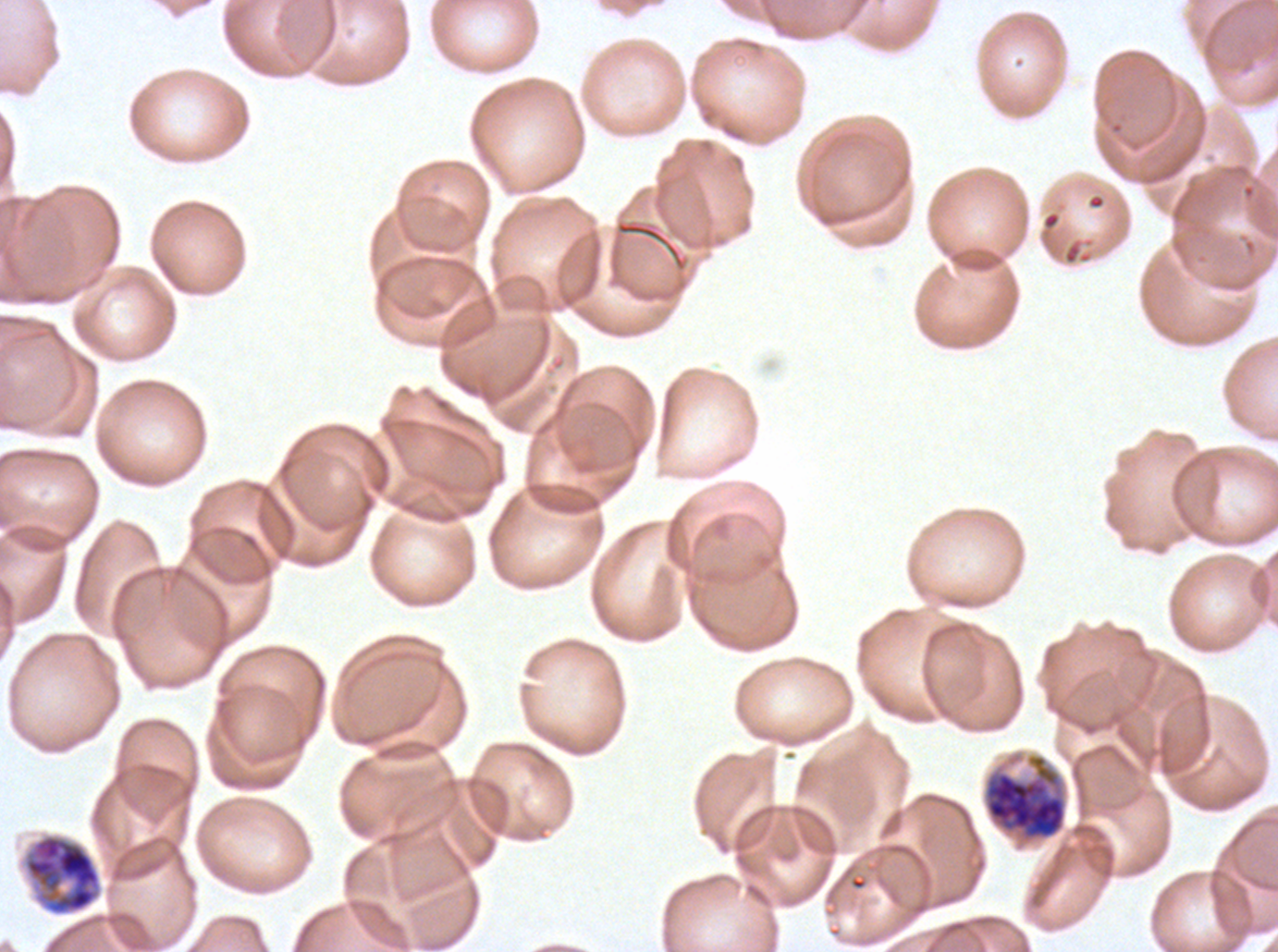

Approximate bounding rectangles given as corner coordinates in pixels from the top-left.
Summary:
  - Late schizont locations: (x1=983, y1=754, x2=1067, y2=841), (x1=22, y1=833, x2=103, y2=917)
  - Specimen: P. falciparum from a patient in The Gambia, cultured ex vivo for 24 to 48 hours
  - Image size: 1278×952 pixels
  - Stain: Giemsa
  - Field of view: one sub-image of a larger composite
  - Preparation: thin blood film